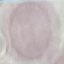
Malaria status: uninfected. Giemsa-stained preparation. Thin blood smear. Cell patch, automatically extracted from a larger field of view and resized to 64 × 64 pixels. Acquired by smartphone through the microscope eyepiece.